Point out each Plasmodium parasite.
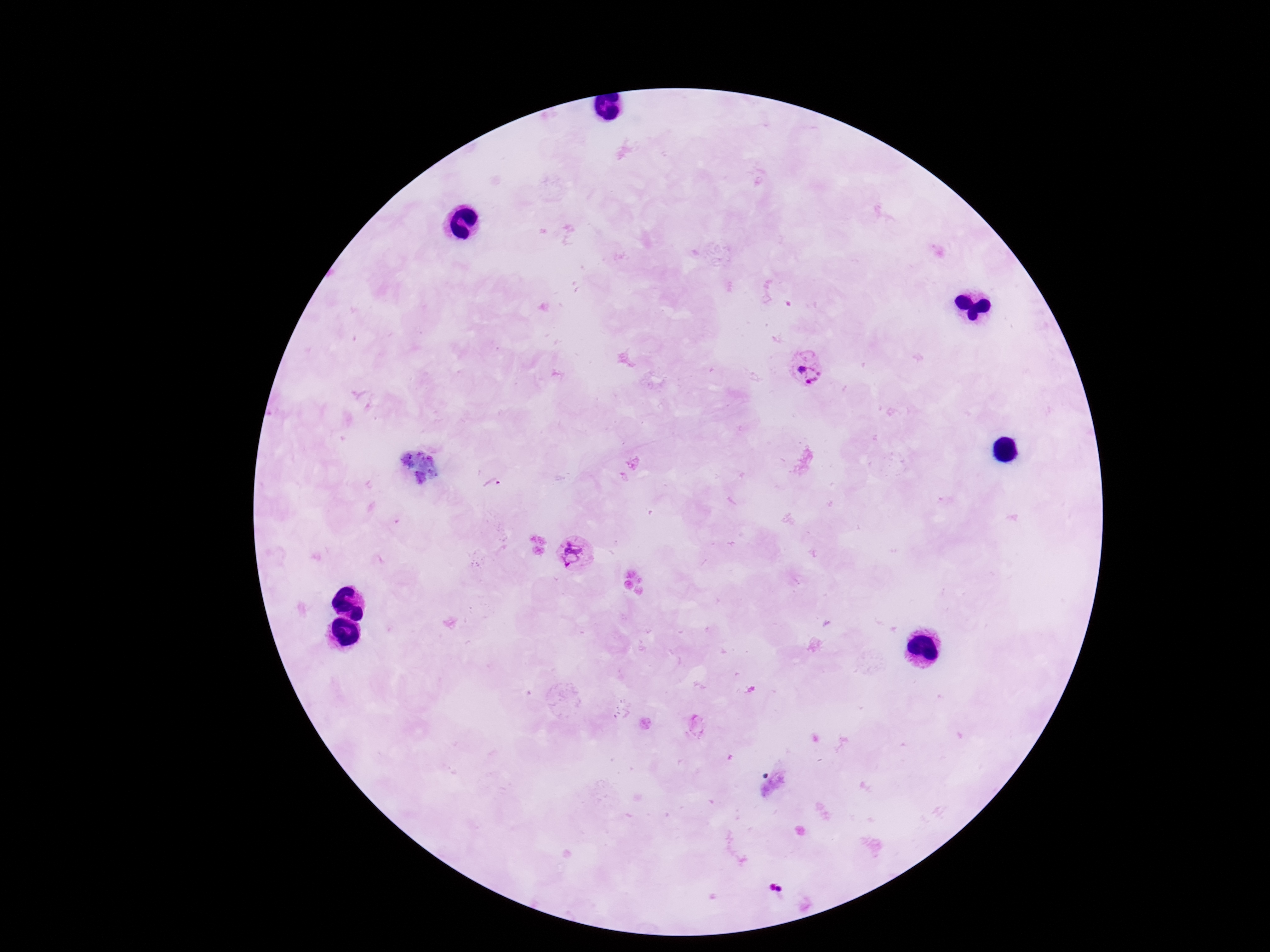

Approximate object centers, in pixels from the top-left corner.
Plasmodium parasites: (x=809, y=368), (x=576, y=555).

Photographed through the microscope eyepiece with a smartphone camera. Thick blood smear. Image is 1270×952 pixels. Patient malaria status: infected. Single field of view. 100x magnification. Giemsa stain.